Identify the preparation type.
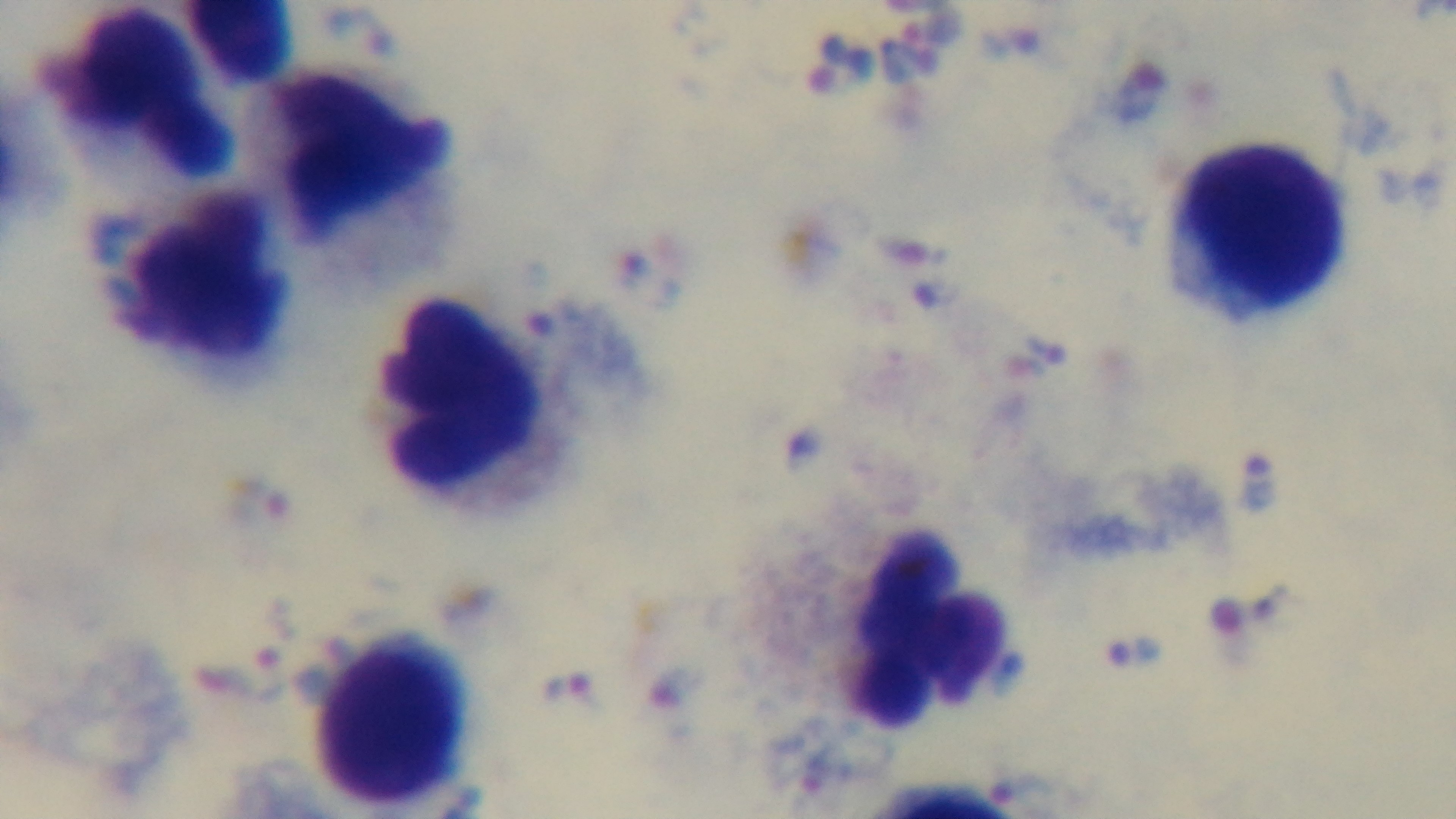
It is a thick blood film.

Light microscopy. Mounted 4K digital camera. Malaria status: infected. One field from the slide. Giemsa stain. Oil-immersion objective, 100x.